Name the cell type shown.
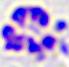
A leukocyte.

Photomicrograph. Captured at 400x magnification.